Describe the morphology of the red blood cells.
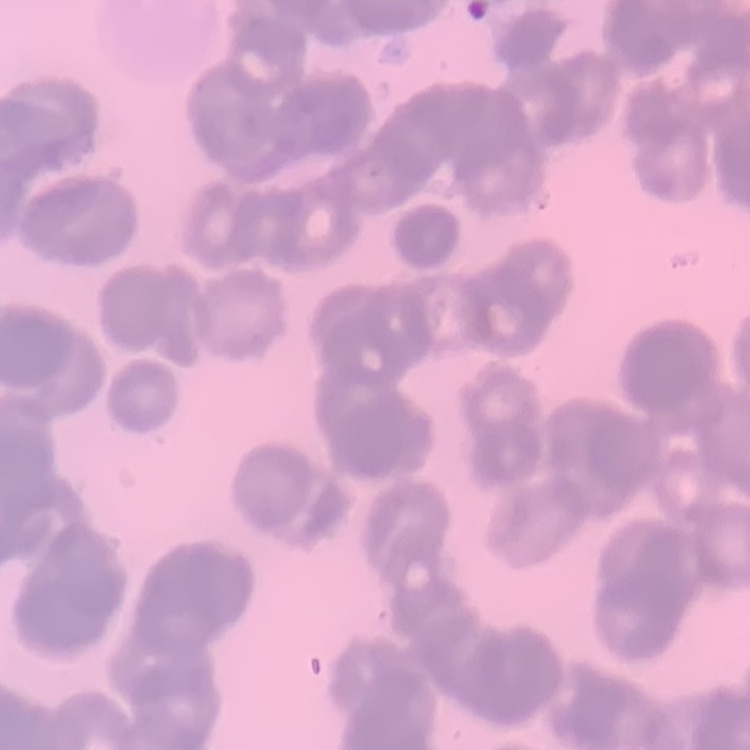
Rouleaux formation.

image type = square crop of a larger photomicrograph
preparation = thin blood smear
stain = Field's or Giemsa